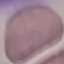
Result: negative for malaria parasites. Thin blood film. Automatically extracted cell patch, resized to 64 × 64 pixels. Giemsa-stained preparation. Photographed with a smartphone camera at the microscope eyepiece.